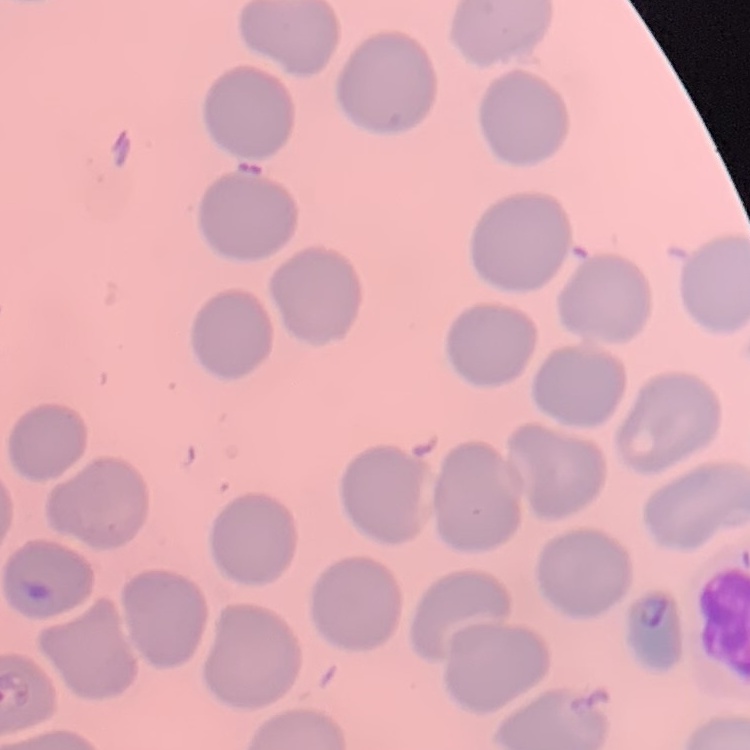

The red blood cells show no rouleaux formation. Stained with either Field's or Giemsa. One tile cut from a larger photomicrograph. Thin peripheral smear.